Locate and identify every blood parasite.
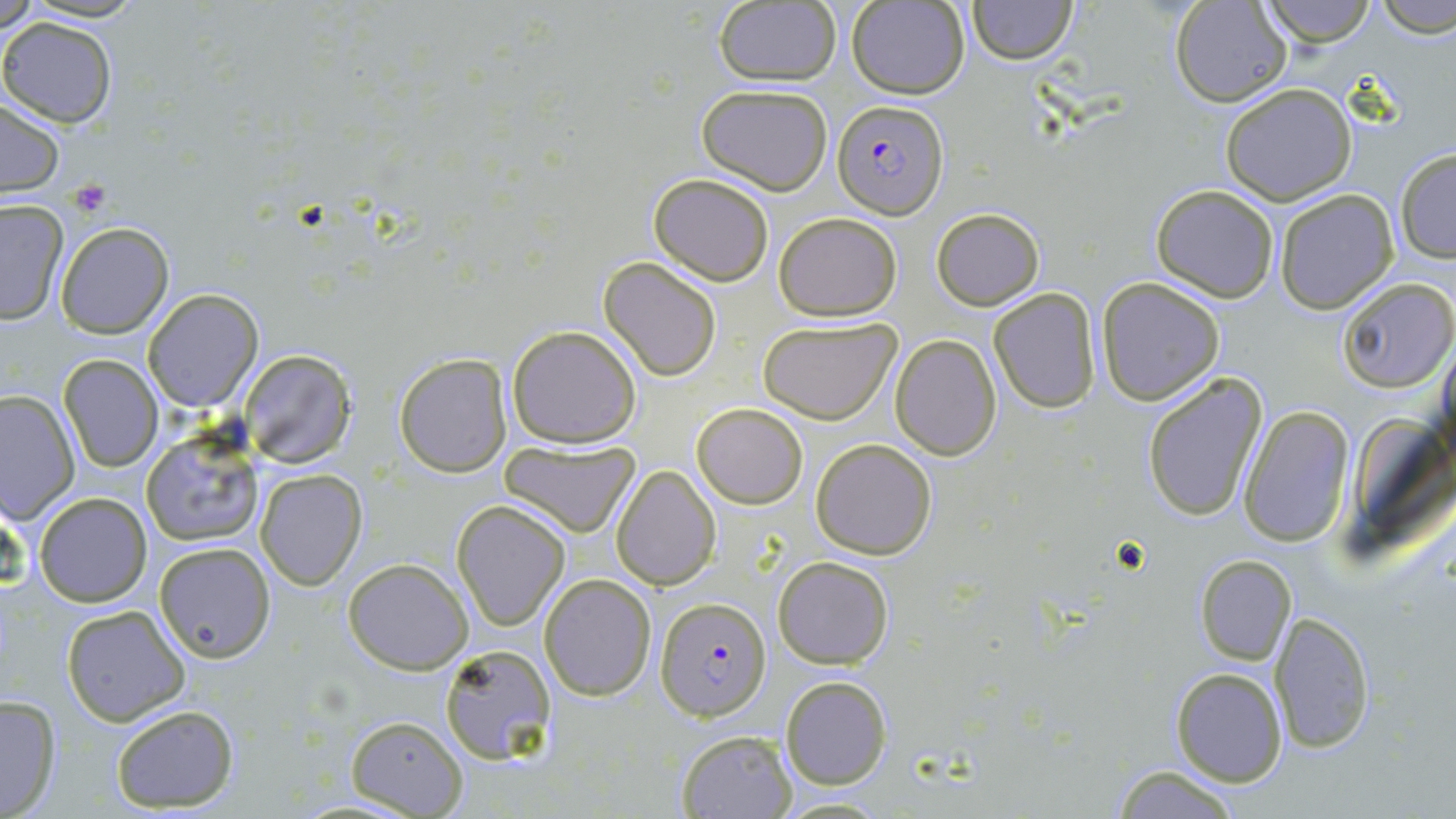
Approximate bounding boxes as named x1/y1/x2/y2 corners in pixels.
Plasmodium falciparum-infected red blood cells: (x1=833, y1=99, x2=948, y2=221), (x1=656, y1=597, x2=771, y2=720).
No Plasmodium ovale, Plasmodium malariae, Plasmodium vivax, Babesia divergens, or Trypanosoma brucei observed.

slide-level diagnosis = Plasmodium falciparum
field of view = single
preparation = thin blood smear
image size = 1456×819 pixels
magnification = 1000x
platelet locations = approximate bounding boxes as named x1/y1/x2/y2 corners in pixels: (x1=68, y1=178, x2=112, y2=217)
modality = light microscopy
stain = May-Grünwald-Giemsa
uninfected red blood cell locations = approximate bounding boxes as named x1/y1/x2/y2 corners in pixels: (x1=0, y1=0, x2=41, y2=34), (x1=847, y1=0, x2=969, y2=99), (x1=968, y1=0, x2=1077, y2=63), (x1=1169, y1=0, x2=1294, y2=108), (x1=1258, y1=0, x2=1381, y2=48), (x1=1372, y1=0, x2=1456, y2=37), (x1=713, y1=1, x2=840, y2=86), (x1=0, y1=17, x2=117, y2=127), (x1=697, y1=83, x2=834, y2=195), (x1=1220, y1=84, x2=1357, y2=205), (x1=1, y1=98, x2=67, y2=199), (x1=1394, y1=146, x2=1456, y2=264), (x1=648, y1=173, x2=774, y2=284), (x1=1150, y1=184, x2=1279, y2=301), (x1=1274, y1=190, x2=1397, y2=313), (x1=0, y1=198, x2=70, y2=324), (x1=932, y1=207, x2=1045, y2=311), (x1=774, y1=211, x2=902, y2=321), (x1=55, y1=220, x2=173, y2=337), (x1=598, y1=257, x2=722, y2=381), (x1=1097, y1=277, x2=1225, y2=406), (x1=1338, y1=278, x2=1455, y2=392), (x1=988, y1=287, x2=1102, y2=413), (x1=144, y1=289, x2=264, y2=412), (x1=757, y1=315, x2=900, y2=423), (x1=506, y1=324, x2=641, y2=448), (x1=890, y1=333, x2=1000, y2=459), (x1=239, y1=349, x2=358, y2=468), (x1=394, y1=351, x2=512, y2=476), (x1=58, y1=354, x2=164, y2=472), (x1=1140, y1=372, x2=1267, y2=523), (x1=1, y1=391, x2=78, y2=523), (x1=691, y1=403, x2=808, y2=509), (x1=1239, y1=405, x2=1355, y2=547), (x1=142, y1=428, x2=262, y2=546), (x1=810, y1=439, x2=937, y2=560), (x1=501, y1=440, x2=637, y2=537), (x1=611, y1=466, x2=719, y2=590), (x1=256, y1=468, x2=368, y2=589), (x1=34, y1=492, x2=153, y2=607), (x1=453, y1=500, x2=570, y2=629), (x1=154, y1=542, x2=276, y2=664), (x1=1194, y1=555, x2=1296, y2=666), (x1=772, y1=556, x2=894, y2=670), (x1=344, y1=558, x2=472, y2=674), (x1=540, y1=573, x2=656, y2=700), (x1=61, y1=603, x2=190, y2=725), (x1=1270, y1=610, x2=1377, y2=754), (x1=439, y1=644, x2=557, y2=762), (x1=1169, y1=667, x2=1287, y2=787), (x1=780, y1=675, x2=892, y2=790), (x1=0, y1=693, x2=63, y2=819), (x1=109, y1=704, x2=240, y2=811), (x1=344, y1=715, x2=468, y2=817), (x1=675, y1=729, x2=796, y2=818), (x1=1110, y1=766, x2=1246, y2=818)